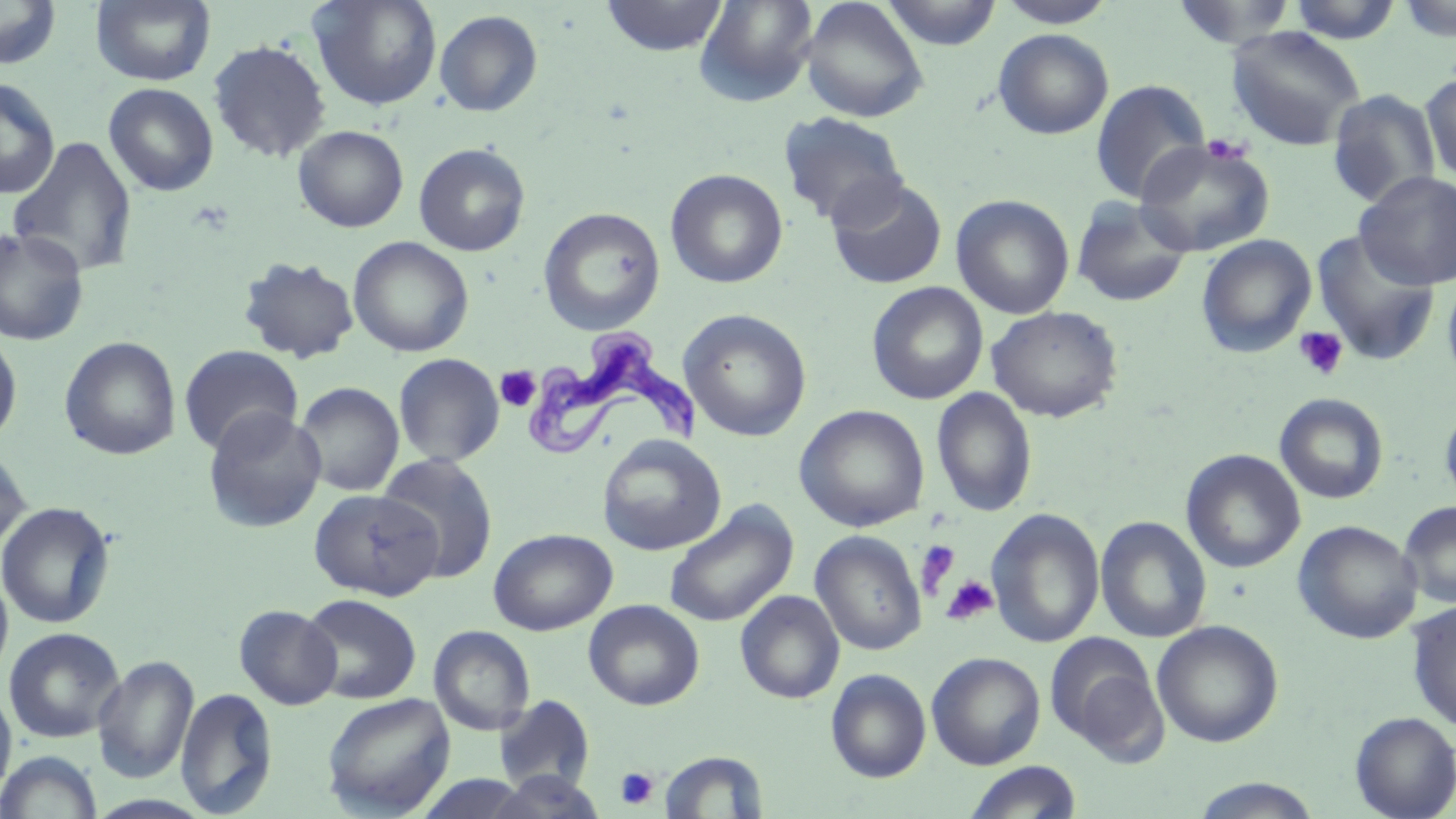
Summary:
  - Coordinate format: approximate bounding boxes as [x1, y1, x2, y2] in pixels
  - Uninfected red blood cell locations: [91, 0, 216, 86], [308, 0, 443, 111], [600, 0, 728, 57], [694, 0, 819, 107], [880, 0, 1003, 50], [996, 0, 1117, 28], [1285, 0, 1404, 44], [0, 1, 62, 70], [799, 1, 928, 122], [1169, 1, 1298, 50], [1397, 1, 1456, 43], [434, 10, 543, 117], [1225, 25, 1366, 151], [993, 28, 1114, 140], [208, 39, 331, 163], [1419, 71, 1456, 184], [0, 78, 60, 199], [1089, 79, 1210, 204], [103, 83, 219, 196], [1326, 89, 1442, 208], [778, 111, 908, 228], [293, 125, 408, 232], [1134, 135, 1276, 257], [6, 136, 139, 278], [413, 143, 531, 256], [665, 168, 788, 288], [1354, 171, 1456, 289], [826, 177, 948, 289], [951, 194, 1074, 319], [1070, 196, 1193, 308], [538, 207, 665, 335], [0, 228, 90, 346], [1310, 229, 1441, 367], [1195, 234, 1317, 359], [348, 236, 474, 357], [237, 256, 360, 364], [1442, 273, 1456, 391], [866, 282, 988, 405], [986, 305, 1123, 422], [678, 309, 812, 442], [0, 331, 22, 448], [59, 335, 182, 461], [178, 345, 303, 456], [393, 353, 505, 466], [294, 381, 404, 497], [931, 387, 1037, 518], [1274, 393, 1389, 505], [1439, 399, 1456, 513], [794, 404, 930, 532], [203, 407, 327, 533], [597, 434, 726, 556], [0, 446, 31, 556], [1181, 449, 1306, 574], [376, 452, 499, 583], [308, 488, 442, 601], [0, 501, 116, 629], [1398, 501, 1456, 609], [664, 502, 799, 627], [986, 507, 1104, 649], [1095, 516, 1212, 644], [1293, 520, 1422, 644], [488, 528, 617, 635], [810, 531, 926, 656], [0, 568, 14, 687], [735, 590, 844, 704], [300, 593, 422, 704], [583, 600, 704, 710], [1406, 601, 1456, 731], [234, 604, 342, 710], [1151, 620, 1284, 748], [429, 626, 535, 736], [4, 627, 125, 743], [1045, 633, 1167, 762], [926, 651, 1046, 769], [92, 655, 199, 784], [825, 668, 932, 783], [0, 684, 16, 802], [175, 687, 278, 816], [322, 692, 456, 818], [494, 695, 595, 792], [1350, 711, 1456, 818], [0, 750, 103, 818], [658, 750, 769, 818], [963, 761, 1082, 819], [488, 772, 606, 819], [1187, 777, 1325, 818], [85, 793, 214, 818]
  - Trypanosoma brucei locations: [523, 327, 705, 458]
  - Platelet locations: [1201, 136, 1253, 166], [1293, 326, 1349, 382], [496, 366, 540, 412], [915, 540, 960, 598], [940, 575, 998, 625], [615, 767, 659, 809]
  - Slide-level diagnosis: Trypanosoma brucei
  - Modality: optical microscopy
  - Stain: May-Grünwald-Giemsa
  - Preparation: thin blood film
  - Field of view: one of a larger specimen
  - Magnification: 1000x
  - Image size: 1456×819 pixels